Classify this cell by malaria status.
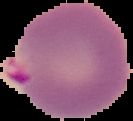
Parasitized.

Image is 133×121 pixels. Cell region segmented out of the field of view; the surrounding area is masked to black. From a thin blood smear.